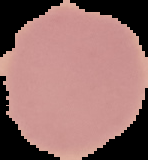

Summary:
  - Image type: segmented cell region with the area outside set to black
  - Preparation: thin blood smear
  - Result: no Plasmodium parasites seen
  - Image size: 148×160 pixels